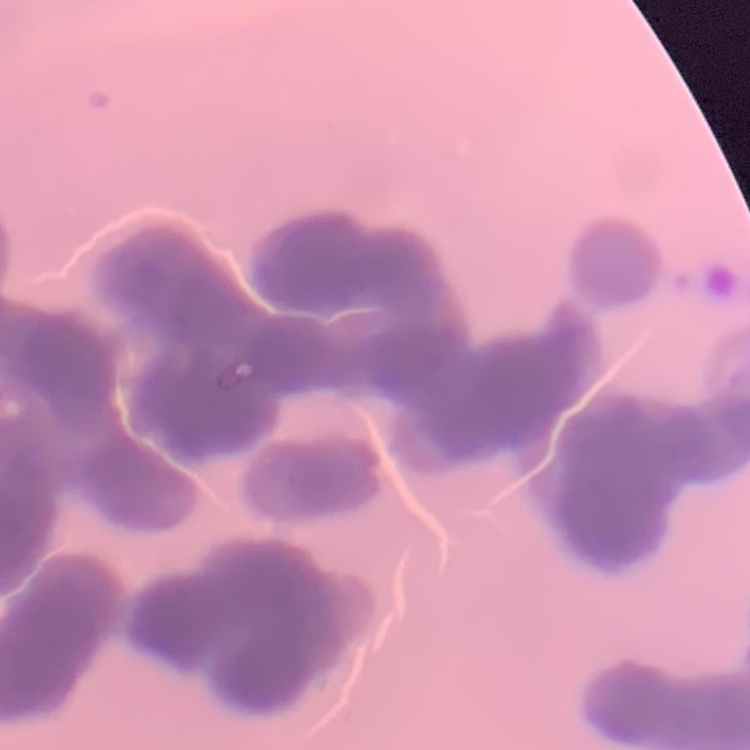

The red blood cells show rouleaux formation. Square crop of a larger photomicrograph. Thin peripheral smear. Field's or Giemsa stain.